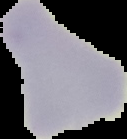

Image is 127×139 pixels. Result: no malaria parasites seen. The area outside the segmented cell region is set to black. From a thin blood smear.